Describe the morphology of the red blood cells.
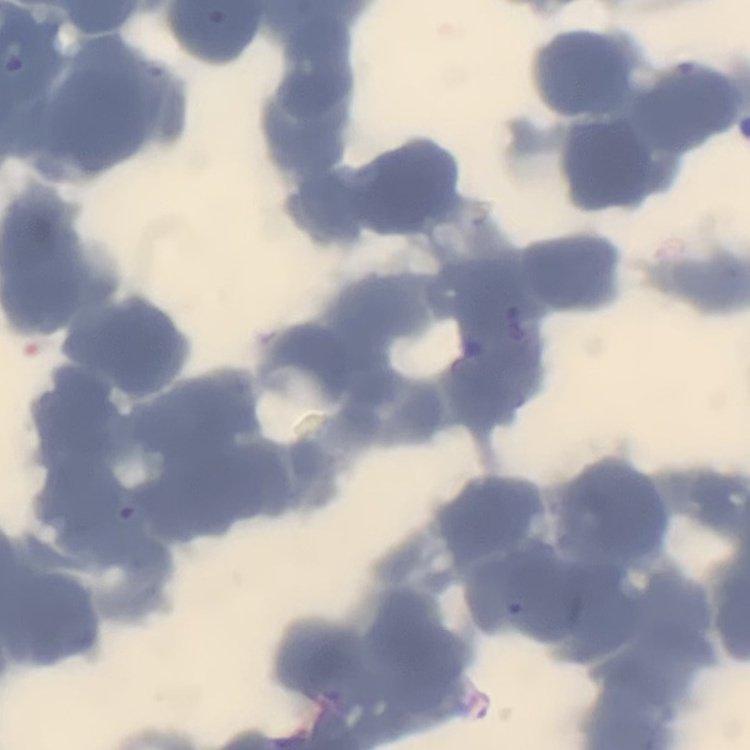
Rouleaux formation.

stain = Field's or Giemsa
preparation = thin blood smear
image type = square crop of a larger photomicrograph